Name the parasite shown.
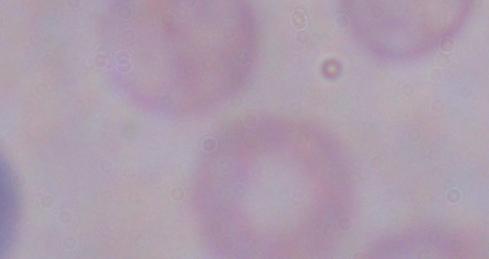

A trypanosome.

Micrograph. 1000x magnification.